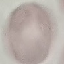

{
  "malaria_status": "uninfected",
  "capture": "smartphone through the microscope eyepiece",
  "image_type": "cell patch, automatically extracted from a larger field of view and resized to 64 × 64 pixels",
  "stain": "Giemsa",
  "preparation": "thin blood smear"
}